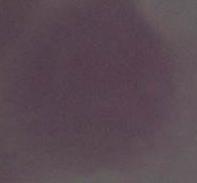

A red blood cell is seen. Micrograph. 1000x magnification.